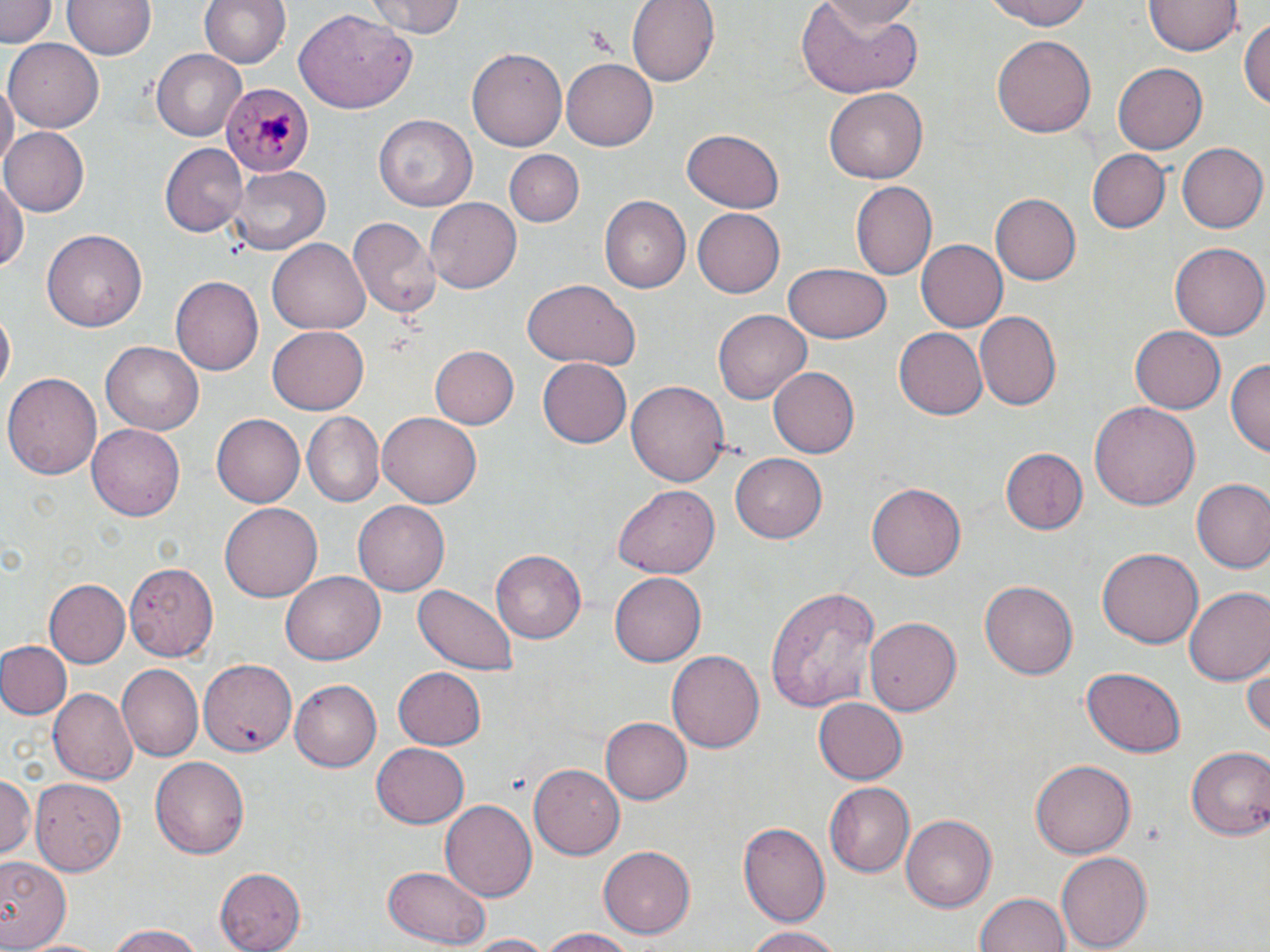
Summary:
  - Coordinate format: approximate bounding boxes as [x1, y1, x2, y2] in pixels
  - Plasmodium malariae-infected red blood cell locations: [224, 80, 313, 179]
  - Uninfected red blood cell locations: [1, 0, 55, 51], [64, 0, 154, 61], [199, 0, 289, 72], [367, 0, 466, 40], [626, 0, 720, 87], [819, 0, 918, 35], [981, 0, 1100, 29], [1146, 0, 1239, 58], [796, 1, 924, 99], [296, 11, 417, 114], [1240, 17, 1270, 114], [991, 35, 1096, 139], [6, 39, 103, 130], [468, 47, 567, 151], [152, 50, 247, 140], [561, 57, 657, 150], [1114, 64, 1207, 153], [1, 78, 17, 176], [826, 88, 927, 182], [375, 115, 477, 212], [0, 127, 88, 217], [681, 130, 784, 214], [1176, 142, 1267, 233], [161, 145, 244, 236], [505, 148, 585, 226], [1088, 150, 1169, 232], [229, 166, 330, 256], [0, 178, 27, 276], [850, 180, 938, 282], [991, 193, 1082, 284], [598, 197, 689, 294], [425, 198, 521, 295], [691, 208, 783, 298], [347, 218, 441, 317], [41, 229, 150, 333], [270, 239, 370, 333], [914, 239, 1006, 332], [1170, 241, 1269, 339], [784, 264, 891, 343], [171, 276, 263, 376], [520, 279, 638, 371], [1, 309, 14, 392], [713, 309, 810, 404], [976, 310, 1063, 411], [1130, 326, 1226, 416], [267, 327, 369, 414], [894, 327, 987, 419], [102, 341, 203, 434], [427, 344, 519, 431], [538, 356, 632, 447], [1228, 361, 1269, 461], [770, 366, 860, 459], [4, 371, 102, 482], [627, 379, 729, 487], [1087, 402, 1199, 514], [300, 411, 383, 504], [378, 413, 481, 507], [212, 414, 305, 507], [88, 423, 183, 522], [1000, 448, 1088, 537], [732, 452, 831, 544], [1192, 478, 1270, 571], [613, 482, 722, 578], [867, 482, 965, 580], [354, 500, 449, 596], [220, 502, 322, 602], [489, 549, 588, 643], [1097, 549, 1202, 650], [123, 560, 217, 662], [610, 569, 705, 663], [281, 572, 383, 664], [45, 579, 130, 668], [980, 579, 1077, 681], [410, 584, 520, 676], [765, 585, 881, 709], [1185, 587, 1270, 684], [865, 617, 961, 716], [0, 640, 72, 718], [668, 651, 764, 753], [1245, 659, 1270, 742], [200, 661, 297, 755], [119, 665, 202, 759], [391, 668, 486, 750], [1082, 668, 1184, 757], [291, 679, 380, 772], [48, 687, 138, 783], [813, 697, 908, 784], [599, 717, 690, 805], [371, 742, 468, 828], [1185, 744, 1269, 840], [150, 757, 248, 860], [1030, 758, 1137, 859], [528, 763, 624, 860], [0, 771, 34, 866], [31, 775, 126, 875], [824, 783, 913, 878], [440, 799, 536, 904], [900, 815, 996, 911], [738, 820, 830, 926], [599, 846, 695, 941], [1055, 850, 1152, 952], [0, 856, 70, 950], [384, 862, 489, 948], [215, 865, 308, 951], [974, 890, 1072, 951], [103, 924, 206, 952], [744, 924, 842, 952], [538, 926, 636, 952], [464, 933, 555, 952], [21, 934, 107, 952]
  - Slide-level diagnosis: Plasmodium malariae
  - Magnification: 1000x
  - Preparation: thin blood film
  - Image size: 1270×952 pixels
  - Modality: light microscopy
  - Field of view: single
  - Stain: May-Grünwald-Giemsa